Outline each blood parasite and name the species.
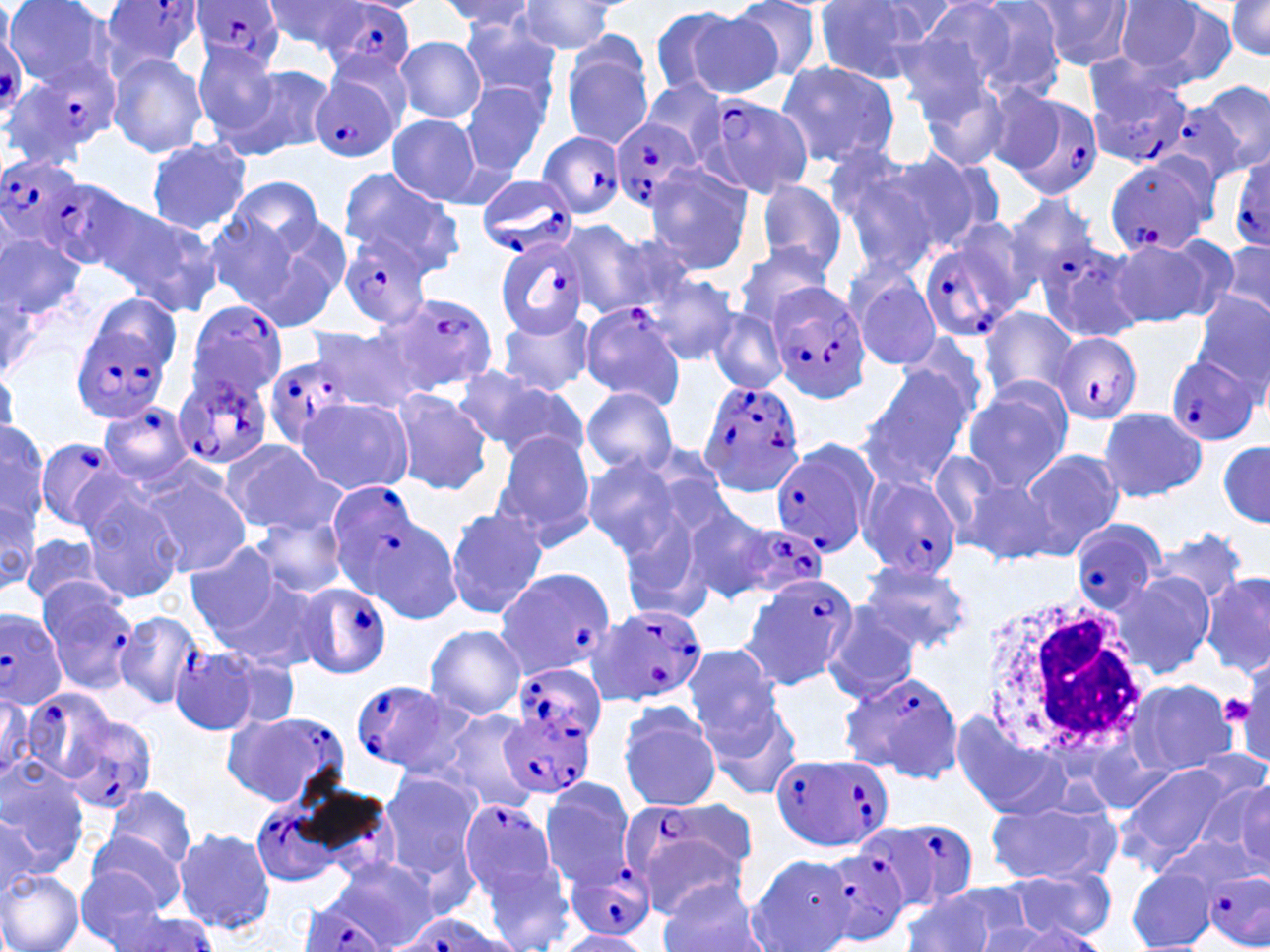
Approximate bounding boxes as (x1,y1)-(x2,y2) corner pairs in pixels.
Plasmodium falciparum-infected red blood cells (subset): (99,0)-(204,74), (188,1)-(284,72), (324,3)-(417,81), (2,61)-(117,166), (1082,66)-(1195,169), (307,75)-(398,163), (999,90)-(1106,200), (701,93)-(816,200), (607,116)-(705,214), (537,131)-(625,220), (1229,151)-(1270,253), (0,153)-(89,260), (1105,157)-(1216,258), (475,173)-(576,261), (52,178)-(135,269), (1004,191)-(1103,291), (920,228)-(1030,341), (341,230)-(436,329), (494,234)-(590,341), (767,283)-(871,401), (386,292)-(498,393), (184,299)-(292,403), (579,301)-(687,407), (73,323)-(173,424), (1049,334)-(1141,425), (262,352)-(359,454), (1167,355)-(1259,445), (173,374)-(273,470), (697,377)-(807,497), (95,402)-(196,483), (33,437)-(130,533), (770,444)-(873,556), (859,475)-(963,581), (1070,518)-(1167,613), (732,525)-(828,601), (492,568)-(615,682), (740,574)-(857,689), (34,579)-(148,694), (294,582)-(391,682), (591,603)-(708,708), (0,607)-(68,710), (168,647)-(265,737), (514,664)-(607,751), (838,670)-(963,782), (22,687)-(119,784), (226,709)-(351,808), (501,711)-(596,800), (65,714)-(157,811), (771,752)-(893,853), (249,798)-(354,888), (457,798)-(559,900), (627,807)-(755,916), (868,820)-(979,910), (819,849)-(910,945), (564,858)-(658,942), (1205,866)-(1270,950), (296,899)-(391,952), (396,914)-(514,952).
No Plasmodium ovale, Plasmodium malariae, Plasmodium vivax, Babesia divergens, or Trypanosoma brucei observed.

slide_level_diagnosis: Plasmodium falciparum
stain: May-Grünwald-Giemsa
field_of_view: one of a larger specimen
uninfected_red_blood_cell_locations_subset: 'approximate bounding boxes as (x1,y1)-(x2,y2) corner pairs in pixels: (4,0)-(118,90), (262,0)-(369,54), (439,0)-(541,35), (730,0)-(824,84), (951,0)-(1070,101), (1028,0)-(1135,70), (512,1)-(625,56), (863,1)-(968,48), (1112,1)-(1213,77), (814,2)-(936,83), (1226,2)-(1270,57), (653,7)-(775,99), (893,8)-(1015,119), (458,15)-(565,109), (395,35)-(486,123), (561,44)-(655,151), (192,46)-(284,143), (106,52)-(207,158), (773,61)-(901,170), (230,62)-(334,159), (912,69)-(1022,174), (639,79)-(728,163), (1192,81)-(1269,178), (460,84)-(549,178), (386,114)-(483,204), (145,136)-(252,233), (883,148)-(1002,256), (824,149)-(938,266), (644,163)-(757,274), (337,165)-(461,267), (229,176)-(325,257), (751,179)-(850,275), (88,195)-(220,315), (205,214)-(300,313), (259,214)-(351,321), (555,218)-(646,320), (0,228)-(86,326), (1107,237)-(1222,330), (1036,240)-(1146,345), (1217,242)-(1270,320), (732,245)-(835,330), (847,268)-(944,370), (639,270)-(740,366), (1191,291)-(1270,392), (83,295)-(183,364), (978,307)-(1081,402), (709,309)-(785,392), (498,311)-(596,398), (474,323)-(588,450), (306,325)-(425,412), (449,366)-(552,449), (857,369)-(971,488), (963,378)-(1075,491), (486,382)-(591,467), (580,386)-(678,477), (387,389)-(491,496), (295,396)-(413,496), (1097,407)-(1209,503), (0,422)-(47,527), (532,428)-(644,556), (490,433)-(600,549), (220,439)-(341,535), (1218,441)-(1268,529), (1018,449)-(1123,557), (928,450)-(1011,543), (580,455)-(683,554), (136,466)-(253,577), (962,476)-(1056,565), (76,488)-(185,606), (615,495)-(733,619), (673,498)-(778,606), (0,499)-(38,594), (444,506)-(548,619), (251,513)-(349,599), (1152,529)-(1250,605), (23,532)-(104,605), (183,540)-(287,640), (857,561)-(972,652), (1202,570)-(1270,677), (1111,571)-(1216,677), (220,580)-(324,671), (821,604)-(924,702), (115,609)-(203,708), (423,625)-(527,720), (681,642)-(783,743), (220,653)-(304,731), (1124,679)-(1238,777), (0,690)-(36,783), (617,702)-(723,811), (704,702)-(802,801), (436,709)-(545,814), (951,712)-(1065,820), (0,755)-(91,874), (1116,761)-(1240,866), (378,770)-(480,876), (536,779)-(636,888), (1195,780)-(1269,864), (105,786)-(197,875), (985,793)-(1120,886), (0,813)-(40,903), (173,825)-(276,935), (86,830)-(184,916), (1157,833)-(1259,903), (479,854)-(577,952), (745,855)-(857,952), (325,856)-(444,952), (74,867)-(172,949), (1127,867)-(1217,951), (0,868)-(84,952), (1005,869)-(1114,943), (657,882)-(770,952), (932,882)-(1038,948), (900,893)-(996,952), (108,911)-(217,952), (977,916)-(1089,952), (552,929)-(654,951)'
image_size: 1270×952 pixels
magnification: 1000x
white_blood_cell_locations: 'approximate bounding boxes as (x1,y1)-(x2,y2) corner pairs in pixels: (974,591)-(1146,760)'
modality: optical microscopy
platelet_locations: 'approximate bounding boxes as (x1,y1)-(x2,y2) corner pairs in pixels: (1219,690)-(1256,727)'
preparation: thin blood film